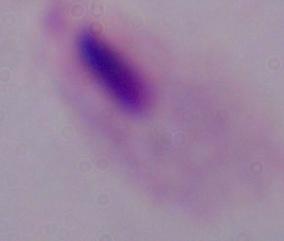
modality = micrograph
magnification = 1000x
identification = trichomonad